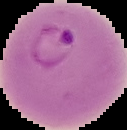 Image is 127×130 pixels. From a thin blood smear. Malaria status: parasitized. Segmented cell region on a black background.